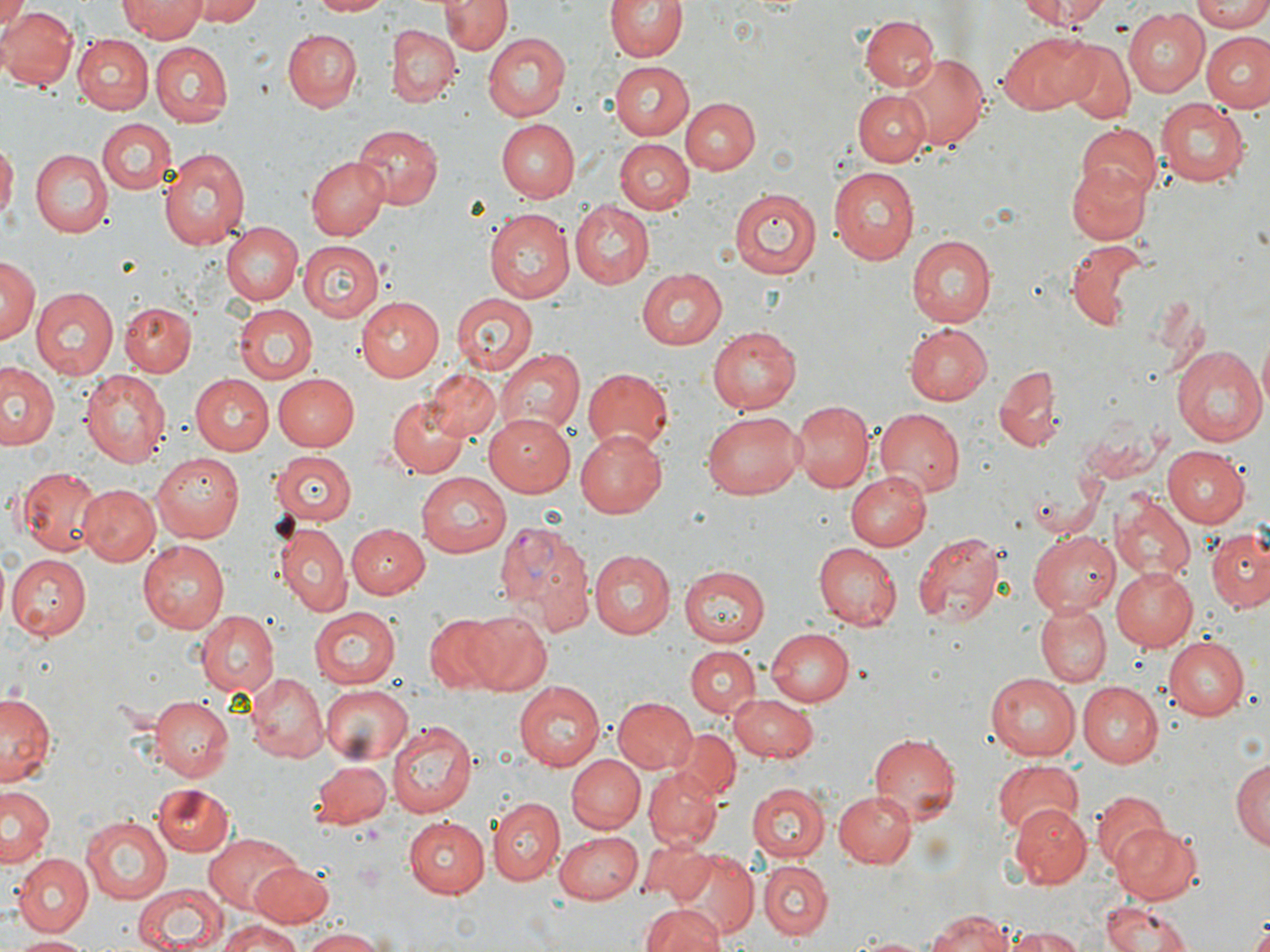 Approximate bounding boxes as (x1,y1)-(x2,y2) corner pairs in pixels. Uninfected red blood cell locations: (191,0)-(268,25), (305,0)-(389,17), (606,0)-(686,63), (1013,0)-(1109,27), (1191,0)-(1270,30), (0,1)-(26,40), (441,1)-(509,56), (121,2)-(205,42), (0,5)-(76,89), (1122,10)-(1208,97), (859,15)-(940,92), (389,24)-(460,106), (282,29)-(362,111), (995,30)-(1097,115), (1203,31)-(1270,110), (75,32)-(153,112), (484,33)-(571,119), (151,43)-(233,125), (1060,43)-(1134,124), (899,52)-(988,152), (613,59)-(695,142), (854,89)-(931,165), (1154,96)-(1250,184), (682,98)-(759,175), (496,118)-(580,205), (97,120)-(173,196), (350,123)-(441,210), (1075,125)-(1161,201), (616,139)-(693,213), (0,141)-(16,228), (160,145)-(251,251), (30,150)-(111,235), (307,154)-(392,240), (1066,162)-(1150,245), (832,166)-(921,264), (728,186)-(820,278), (569,203)-(652,288), (484,209)-(574,303), (220,221)-(303,305), (905,234)-(995,326), (1065,240)-(1150,329), (299,241)-(384,322), (0,255)-(39,345), (634,267)-(726,350), (32,287)-(117,377), (452,293)-(539,376), (356,297)-(443,382), (120,302)-(195,376), (233,303)-(319,384), (903,323)-(990,405), (708,326)-(801,414), (1170,345)-(1267,445), (497,348)-(586,435), (990,361)-(1063,455), (1,364)-(59,451), (580,365)-(673,456), (425,368)-(500,444), (80,370)-(173,468), (271,372)-(359,451), (191,375)-(273,454), (389,395)-(473,478), (792,401)-(873,491), (875,409)-(967,496), (703,412)-(801,499), (484,413)-(576,496), (1081,417)-(1164,486), (576,430)-(669,518), (1160,446)-(1248,527), (271,450)-(356,525), (152,453)-(243,542), (14,465)-(104,554), (845,470)-(930,550), (418,472)-(510,557), (77,485)-(159,566), (1111,497)-(1193,581), (276,523)-(350,613), (347,525)-(429,597), (1027,531)-(1120,614), (1205,531)-(1270,611), (914,532)-(1007,626), (137,538)-(230,631), (814,542)-(901,629), (587,549)-(674,640), (9,553)-(91,640), (678,564)-(770,645), (1109,566)-(1198,650), (1035,602)-(1111,686), (309,607)-(401,687), (460,610)-(550,694), (197,611)-(279,698), (424,615)-(512,692), (767,628)-(855,706), (1162,636)-(1248,718), (684,645)-(760,718), (248,674)-(327,762), (985,674)-(1082,760), (1075,682)-(1162,766), (514,683)-(605,770), (319,685)-(413,765), (1,689)-(59,788), (727,694)-(818,762), (149,696)-(233,779), (613,697)-(699,775), (388,720)-(477,816), (674,728)-(740,798), (867,732)-(960,823), (567,756)-(645,833), (1231,756)-(1268,855), (308,759)-(392,834), (990,759)-(1086,835), (645,768)-(721,848), (746,782)-(828,861), (152,784)-(234,855), (2,785)-(56,868), (1087,790)-(1168,868), (833,791)-(917,868), (488,798)-(563,886), (1009,807)-(1091,889), (81,814)-(173,903), (405,816)-(488,896), (1112,823)-(1201,904), (553,830)-(642,902), (201,832)-(303,912), (641,838)-(711,903), (667,849)-(757,936), (12,854)-(93,936), (758,860)-(832,938), (250,862)-(334,928), (133,882)-(231,952), (1100,899)-(1198,952), (642,903)-(724,952), (923,910)-(1020,952), (217,923)-(306,952), (1008,927)-(1086,952), (295,928)-(390,952), (850,933)-(933,951), (13,934)-(94,951). Plasmodium vivax-infected red blood cell locations: (497,518)-(598,639). Slide-level diagnosis: Plasmodium vivax. Light microscopy. Image is 1270×952 pixels. May-Grünwald-Giemsa-stained preparation. Single field of view. Thin blood film. Captured at 1000x magnification.